Describe the morphology of the erythrocytes.
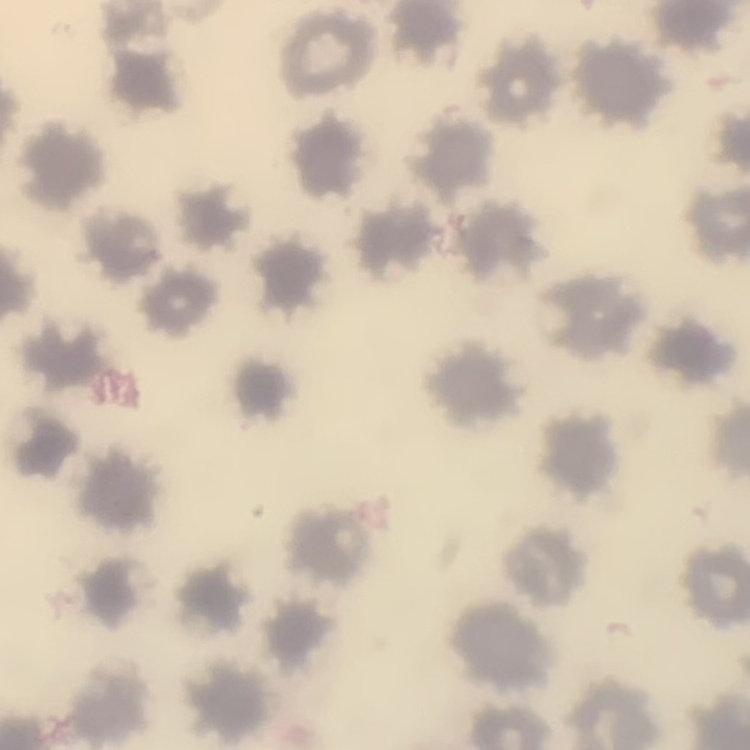
They show no rouleaux formation.

{
  "preparation": "thin peripheral smear",
  "stain": "Field's or Giemsa",
  "image_type": "square crop of a larger photomicrograph"
}